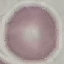
Result: no malaria parasites seen. Giemsa stain. Automatically extracted cell patch, resized to 64 × 64 pixels. Thin blood smear. Acquired by smartphone through the microscope eyepiece.